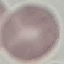

malaria status = uninfected
image type = cell patch, automatically extracted from a larger field of view and resized to 64 × 64 pixels
capture = smartphone through the microscope eyepiece
stain = Giemsa
preparation = thin blood film